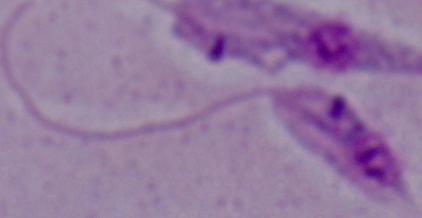
identification = Leishmania
magnification = 1000x
modality = photomicrograph